Locate every Plasmodium parasite.
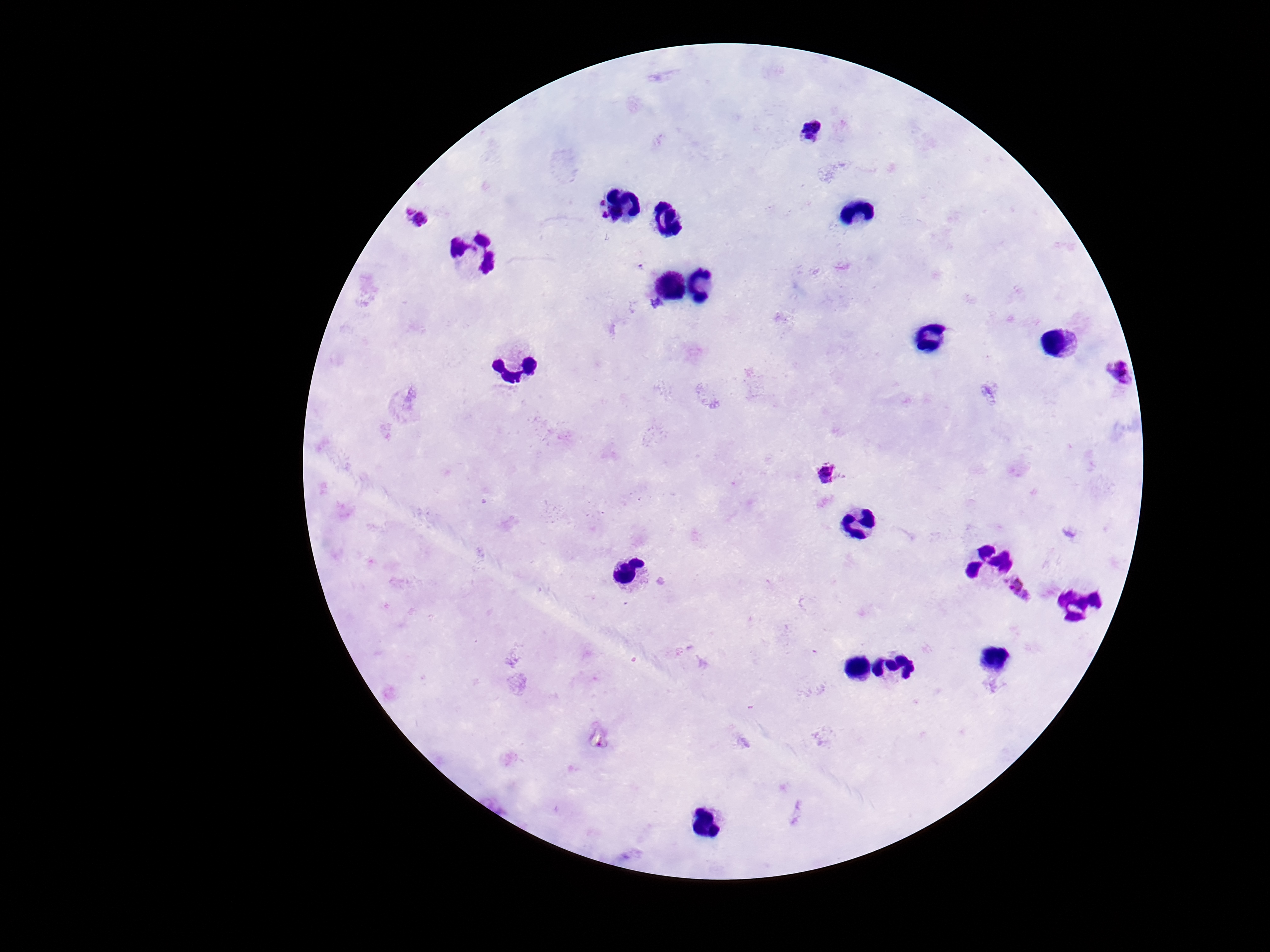

Approximate object centers, in pixels from the top-left corner.
Plasmodium parasites: (x=815, y=131), (x=600, y=203), (x=419, y=218), (x=603, y=218), (x=640, y=266), (x=1116, y=373), (x=829, y=474), (x=1020, y=589).

Smartphone photograph taken through the microscope eyepiece. Patient malaria status: infected. 100x magnification. Image is 1270×952 pixels. Single field of view. Thick peripheral-blood smear. Giemsa-stained preparation.